State which parasite is depicted.
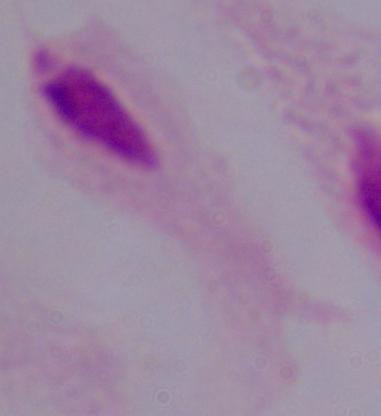

This is a trichomonad.

{
  "magnification": "1000x",
  "modality": "photomicrograph"
}